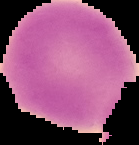

Segmented cell region on a black background. From a thin blood smear. Malaria status: uninfected. Image is 139×145 pixels.